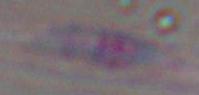
magnification = 1000x
identification = Toxoplasma gondii
modality = photomicrograph